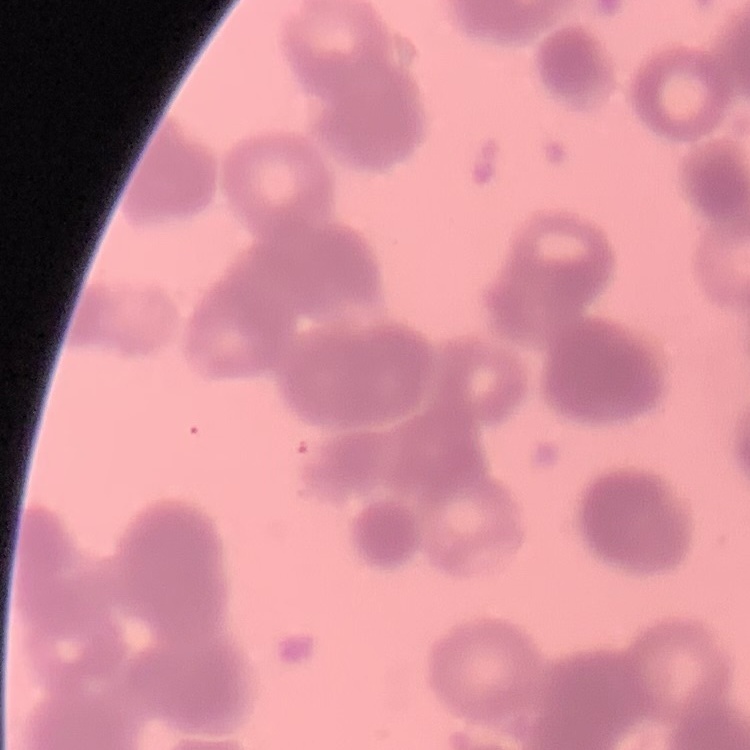

Summary:
  - Erythrocyte morphology: rouleaux formation
  - Stain: Field's or Giemsa
  - Image type: one tile cut from a larger photomicrograph
  - Preparation: thin blood film